Locate every blood parasite and identify its species.
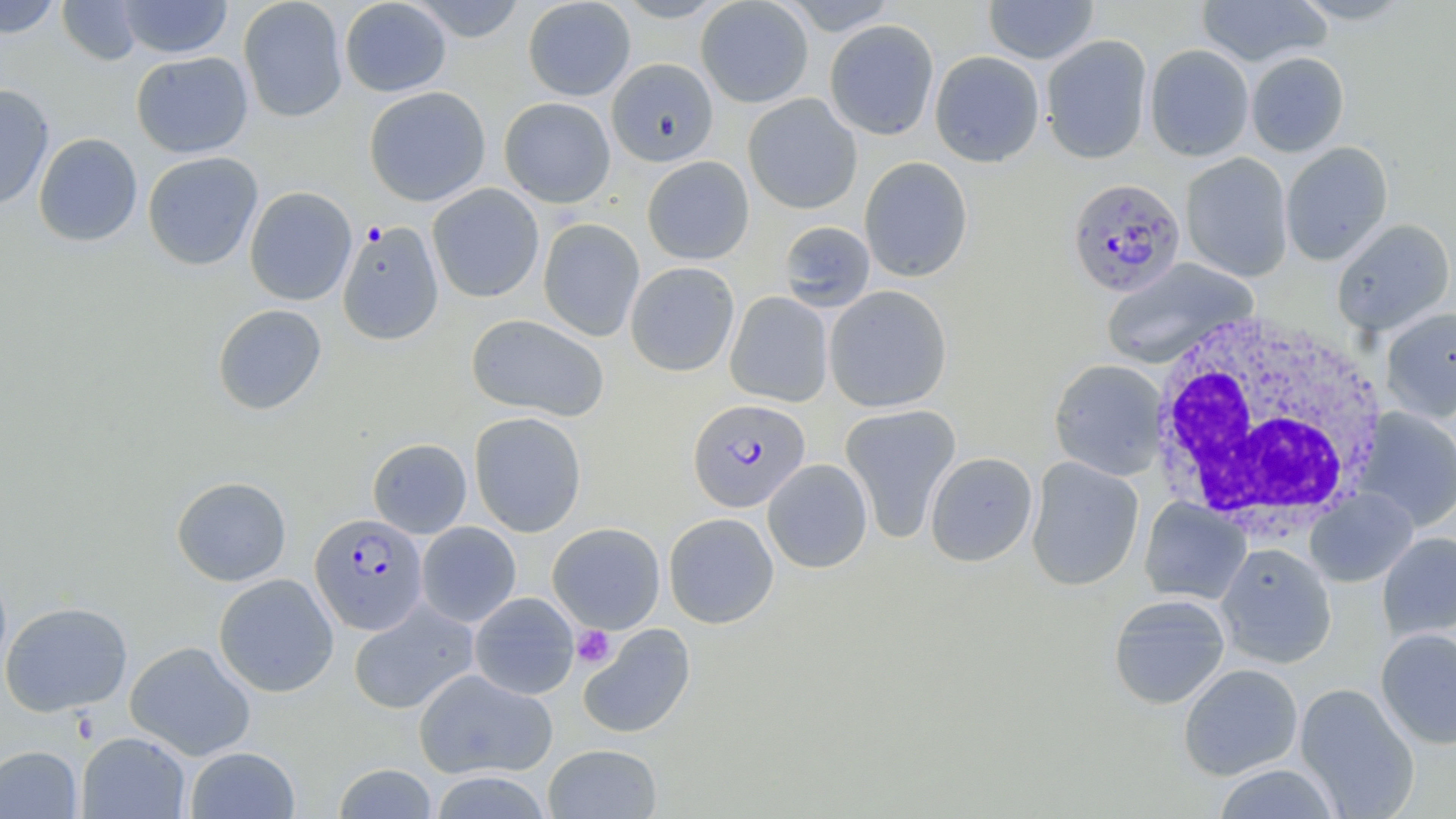

Approximate bounding boxes as [x1, y1, x2, y2] in pixels.
Plasmodium falciparum-infected red blood cells: [1067, 178, 1187, 298], [688, 398, 810, 512], [309, 513, 428, 634].
No Plasmodium ovale, Plasmodium malariae, Plasmodium vivax, Babesia divergens, or Trypanosoma brucei observed.

White blood cell locations: [1148, 308, 1389, 533]. Platelet locations: [572, 625, 616, 669]. Uninfected red blood cell locations: [0, 0, 62, 38], [57, 0, 143, 65], [116, 0, 233, 59], [238, 0, 349, 123], [339, 0, 452, 97], [406, 0, 530, 42], [522, 0, 636, 101], [612, 0, 731, 22], [695, 0, 814, 108], [779, 0, 898, 35], [983, 0, 1100, 64], [1196, 0, 1331, 67], [1289, 0, 1413, 25], [824, 19, 939, 140], [1041, 34, 1152, 164], [1144, 44, 1254, 162], [929, 50, 1045, 167], [131, 51, 253, 158], [1246, 51, 1349, 157], [606, 58, 718, 167], [0, 84, 54, 210], [364, 86, 491, 206], [743, 94, 862, 214], [499, 97, 615, 207], [34, 133, 143, 247], [1280, 141, 1394, 265], [142, 151, 263, 270], [1180, 152, 1293, 282], [642, 156, 754, 265], [859, 156, 973, 283], [427, 184, 544, 303], [244, 186, 357, 306], [537, 218, 645, 342], [1331, 218, 1455, 336], [337, 221, 444, 345], [777, 221, 875, 312], [1101, 257, 1258, 370], [625, 261, 740, 376], [823, 285, 952, 412], [725, 291, 833, 407], [212, 304, 327, 415], [1380, 307, 1456, 423], [466, 313, 609, 421], [1048, 359, 1168, 480], [840, 404, 961, 543], [1356, 408, 1456, 531], [469, 411, 587, 537], [368, 438, 471, 538], [925, 452, 1038, 567], [1026, 457, 1144, 591], [762, 459, 873, 573], [171, 476, 292, 586], [1304, 489, 1418, 587], [1139, 498, 1251, 605], [664, 513, 779, 628], [416, 522, 521, 627], [548, 522, 665, 633], [1377, 532, 1456, 640], [1215, 542, 1337, 668], [0, 560, 12, 687], [213, 573, 339, 697], [469, 592, 579, 700], [1108, 593, 1231, 709], [1, 601, 133, 717], [348, 601, 479, 715], [578, 623, 696, 739], [1375, 628, 1456, 750], [125, 641, 256, 760], [1178, 663, 1303, 780], [413, 668, 557, 780], [1295, 682, 1420, 819], [76, 731, 190, 819], [543, 744, 663, 818], [0, 745, 82, 819], [185, 746, 300, 819], [332, 763, 438, 819], [1211, 763, 1342, 818], [429, 770, 552, 818]. Slide-level diagnosis: Plasmodium falciparum. May-Grünwald-Giemsa-stained preparation. Optical microscopy. Captured at 1000x magnification. Image is 1456×819 pixels. Thin blood smear. One field of a larger specimen.